Locate every Trypanosoma brucei.
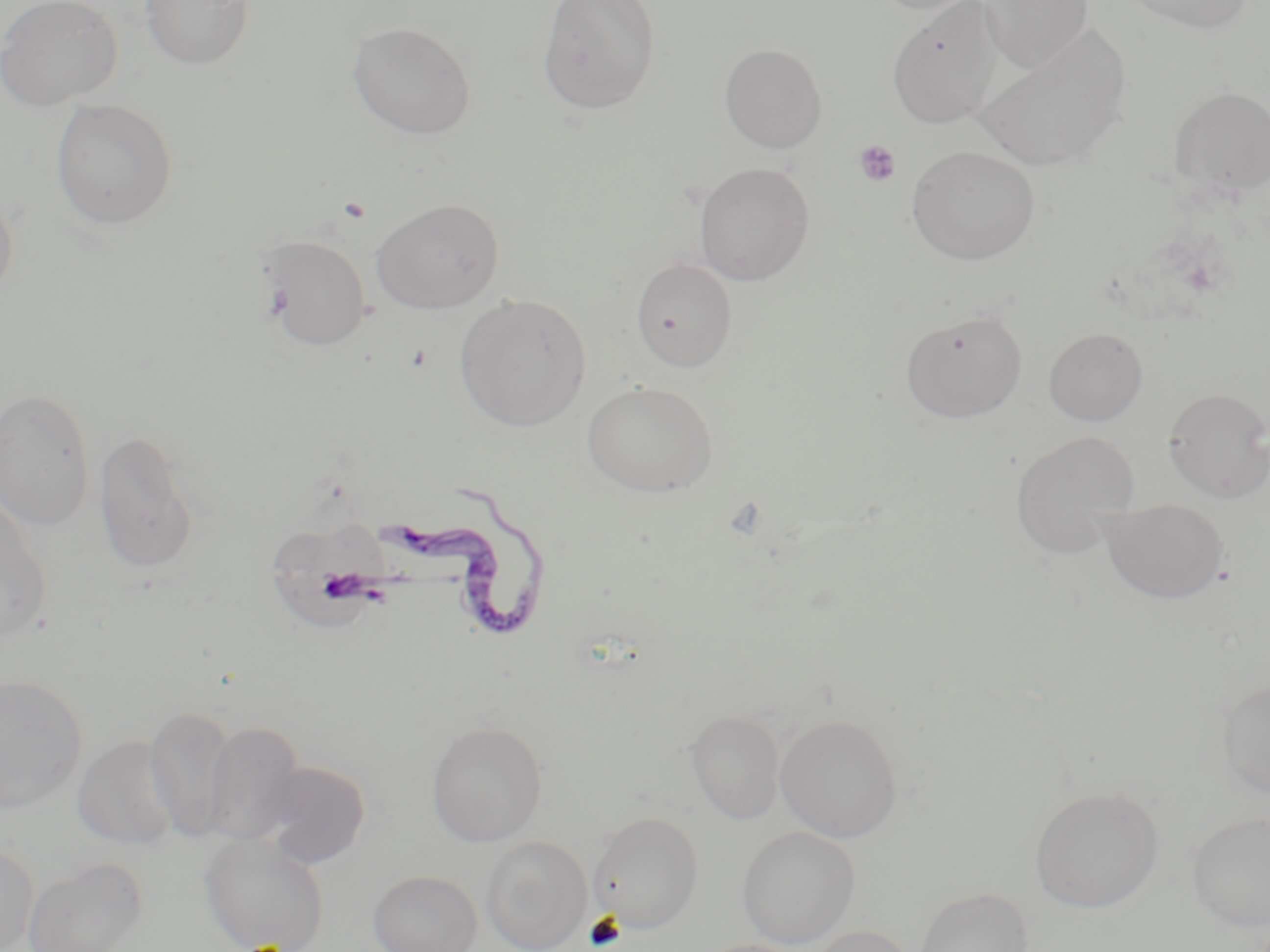
Approximate bounding boxes as (x1, y1, x2, y2) in pixels.
Trypanosoma brucei: (380, 480, 552, 645).

Uninfected red blood cell locations: (0, 0, 122, 111), (140, 0, 254, 70), (537, 0, 661, 114), (870, 0, 990, 16), (979, 0, 1093, 73), (1122, 0, 1255, 33), (887, 2, 1003, 128), (976, 21, 1132, 169), (347, 22, 476, 139), (719, 43, 827, 152), (1170, 85, 1270, 199), (50, 98, 178, 230), (906, 145, 1040, 264), (694, 162, 814, 285), (0, 186, 18, 304), (371, 199, 505, 314), (258, 234, 373, 351), (631, 257, 738, 371), (454, 293, 591, 431), (900, 307, 1028, 422), (1044, 327, 1148, 426), (582, 380, 718, 497), (0, 387, 96, 530), (1163, 388, 1270, 502), (93, 428, 200, 574), (1010, 431, 1139, 559), (0, 495, 52, 642), (1102, 498, 1230, 603), (272, 511, 385, 634), (0, 674, 87, 812), (1217, 679, 1270, 799), (145, 704, 238, 841), (686, 710, 785, 824), (775, 714, 902, 842), (426, 719, 548, 847), (203, 720, 306, 845), (72, 735, 181, 851), (255, 760, 372, 868), (1030, 787, 1163, 912), (588, 810, 704, 932), (1188, 812, 1270, 930), (737, 825, 859, 948), (200, 834, 331, 952), (481, 836, 592, 952), (0, 843, 39, 952), (22, 856, 149, 952), (367, 870, 482, 952), (915, 887, 1033, 952), (805, 925, 918, 952), (694, 938, 809, 952). Platelet locations: (853, 139, 901, 187). Slide-level diagnosis: Trypanosoma brucei. Optical microscopy. May-Grünwald-Giemsa stain. Captured at 1000x magnification. Image is 1270×952 pixels. Thin blood film. Single field of view.